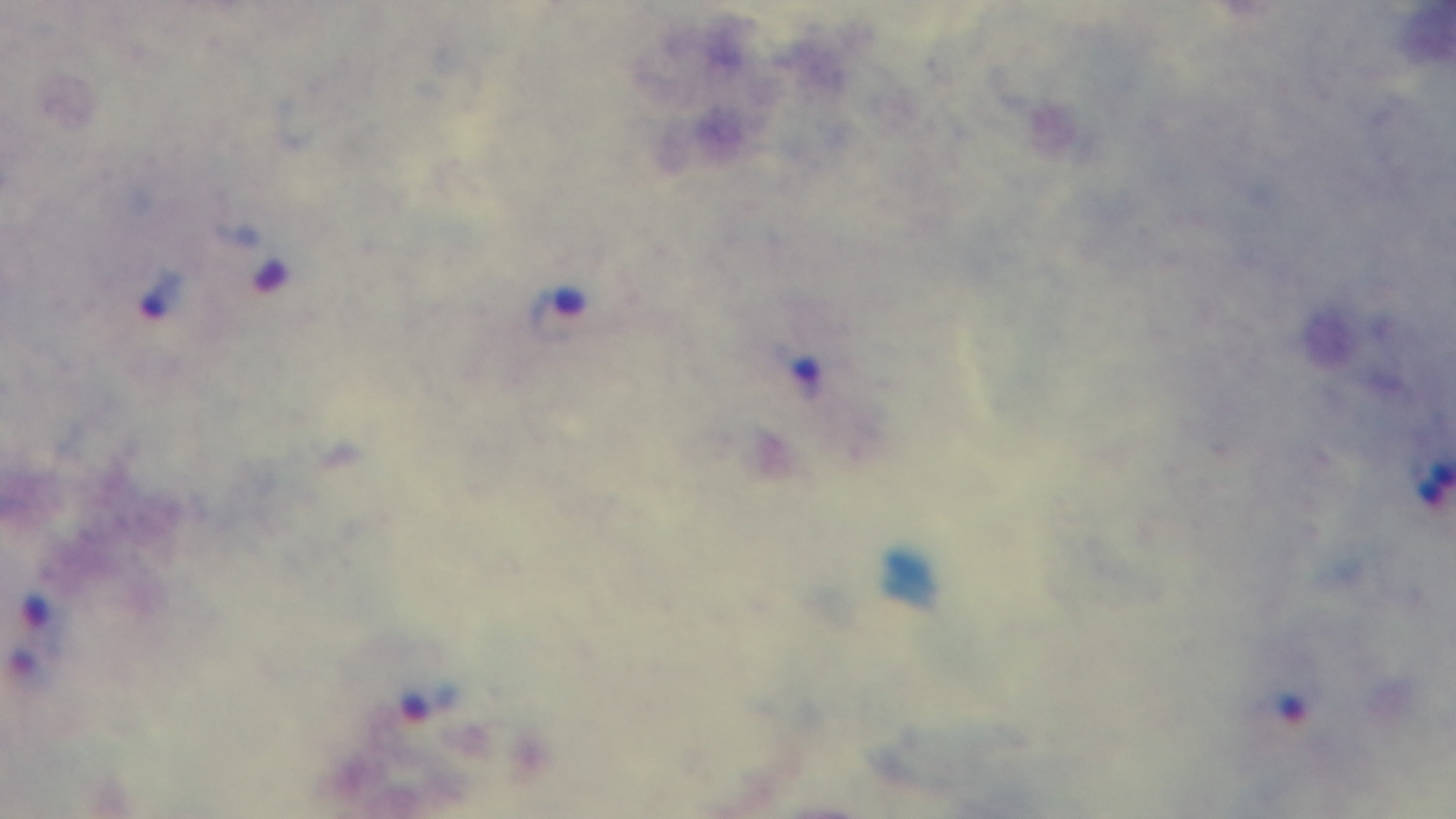
{
  "malaria_status": "infected",
  "stain": "Giemsa",
  "capture": "mounted 4K digital camera",
  "field_of_view": "one from the slide",
  "preparation": "thick blood film",
  "objective": "100x oil immersion",
  "modality": "light microscopy"
}